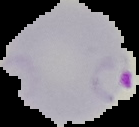

malaria_status: parasitized
preparation: thin blood smear
image_type: segmented cell region with the area outside set to black
image_size: 139×127 pixels